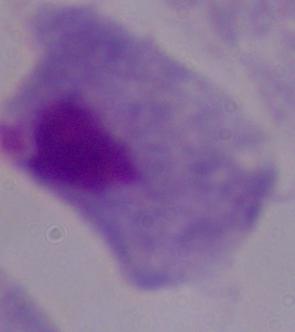 A trichomonad is shown. Photomicrograph. Captured at 1000x magnification.